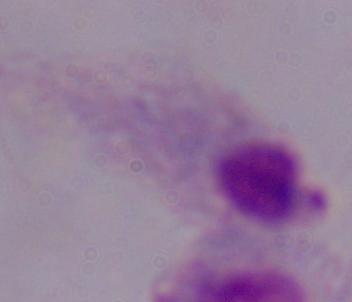

Summary:
  - Modality: photomicrograph
  - Identification: trichomonad
  - Magnification: 1000x